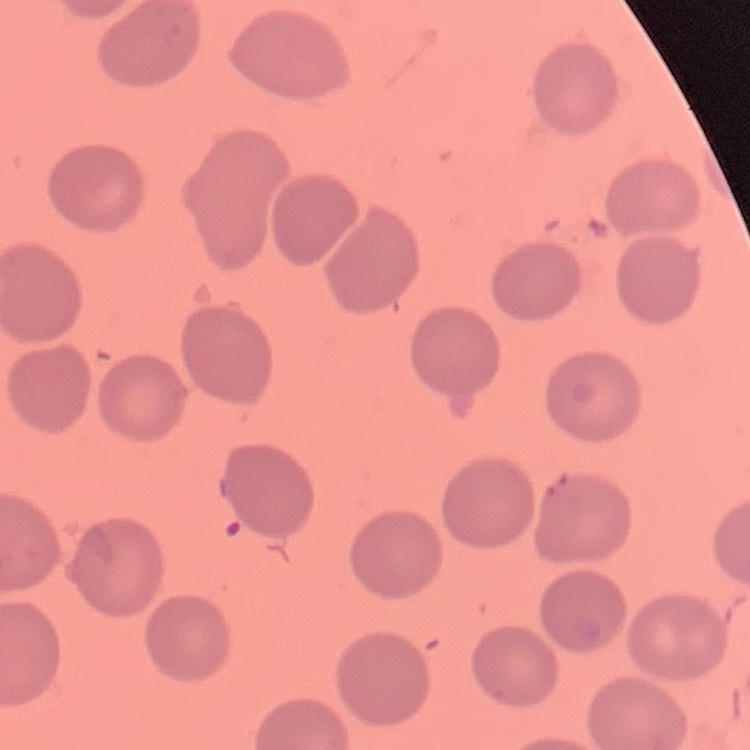
erythrocyte morphology = no rouleaux formation
image type = one tile cut from a larger photomicrograph
preparation = thin peripheral smear
stain = Field's or Giemsa